Assess this cell for malaria.
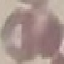

It is uninfected.

Automatically extracted cell patch, resized to 64 × 64 pixels. Thin smear of blood. Acquired by smartphone through the microscope eyepiece. Giemsa-stained preparation.